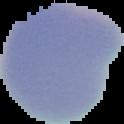 Image is 124×124 pixels. From a thin blood smear. Result: no Plasmodium parasites seen. Segmented cell region on a black background.